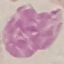
Summary:
  - Result: no malaria parasites seen
  - Image type: cell patch, automatically extracted from a larger field of view and resized to 64 × 64 pixels
  - Preparation: thin smear
  - Stain: Giemsa
  - Capture: smartphone camera at the microscope eyepiece